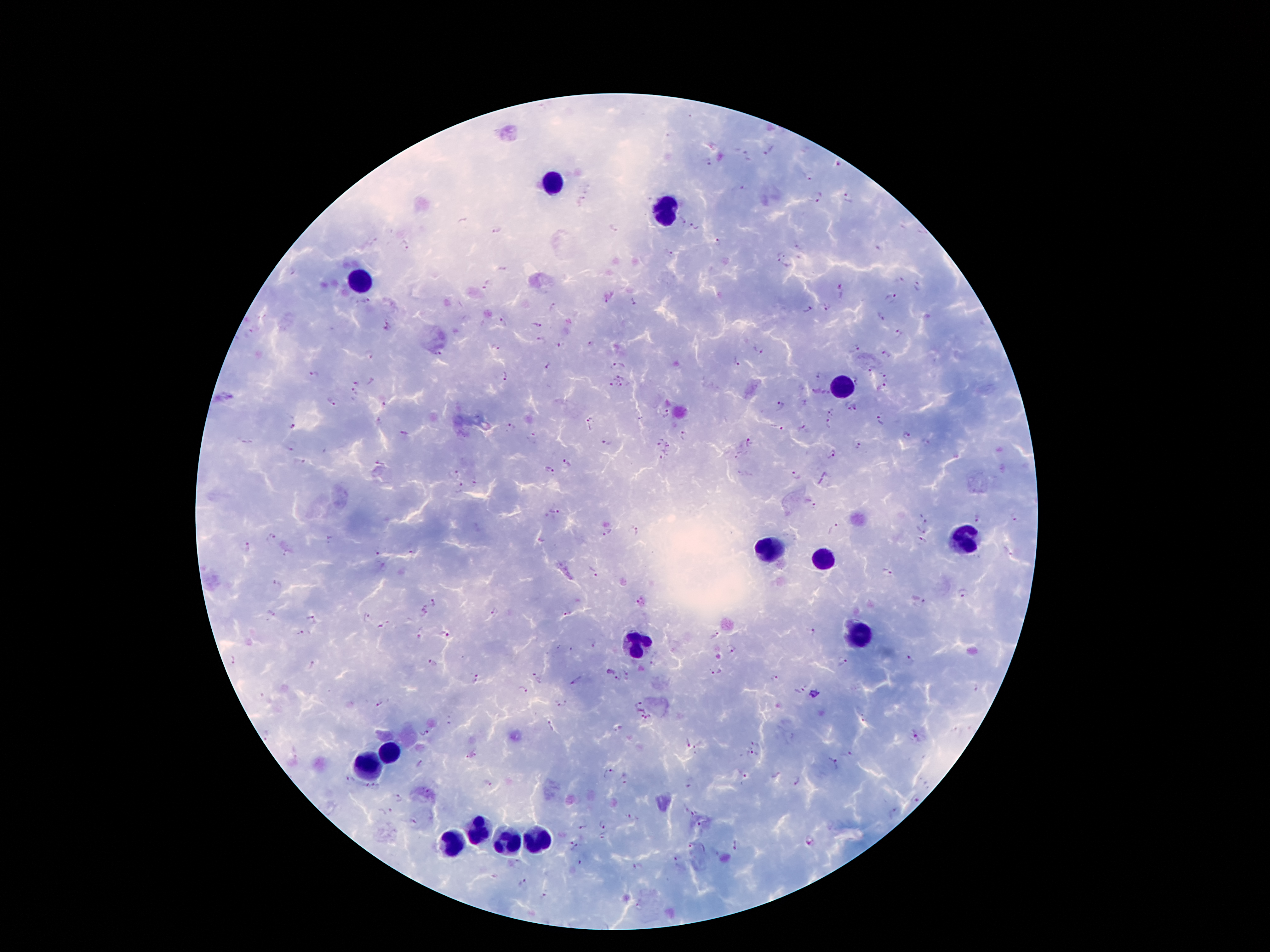

Approximate centers as [x, y] in pixels.
Summary:
  - Plasmodium parasite locations: [769, 152], [746, 157], [707, 163], [839, 165], [810, 177], [820, 197], [849, 197], [580, 200], [462, 221], [683, 221], [694, 226], [614, 228], [497, 231], [718, 243], [404, 247], [782, 250], [879, 251], [672, 252], [782, 265], [503, 270], [901, 279], [487, 284], [919, 285], [842, 291], [891, 296], [609, 298], [635, 300], [552, 304], [827, 308], [806, 310], [881, 316], [504, 323], [535, 326], [388, 328], [900, 333], [541, 341], [590, 343], [561, 346], [496, 348], [757, 348], [857, 348], [368, 354], [438, 354], [887, 354], [620, 362], [736, 362], [548, 366], [872, 368], [315, 373], [817, 374], [883, 374], [623, 375], [505, 378], [857, 380], [355, 383], [613, 384], [623, 386], [883, 387], [815, 391], [354, 392], [828, 392], [332, 402], [385, 404], [780, 405], [857, 406], [846, 407], [831, 411], [667, 412], [881, 419], [591, 423], [828, 425], [291, 426], [511, 427], [777, 429], [804, 429], [404, 434], [684, 434], [907, 436], [533, 438], [660, 439], [750, 440], [244, 442], [608, 442], [858, 444], [669, 445], [290, 449], [831, 454], [665, 455], [740, 455], [298, 463], [381, 463], [567, 463], [549, 471], [454, 474], [797, 475], [476, 482], [462, 490], [810, 503], [554, 509], [978, 517], [1014, 518], [922, 519], [834, 529], [921, 529], [635, 531], [607, 534], [270, 537], [330, 541], [921, 543], [246, 547], [1008, 552], [378, 553], [286, 554], [887, 572], [592, 573], [278, 585], [964, 594], [920, 600], [640, 601], [433, 603], [269, 613], [494, 613], [567, 613], [423, 614], [313, 618], [364, 618], [381, 627], [811, 632], [300, 634], [446, 635], [715, 635], [591, 646], [731, 649], [232, 660], [908, 660], [842, 661], [432, 663], [312, 665], [716, 672], [617, 677], [536, 678], [775, 678], [476, 681], [575, 681], [522, 690], [800, 691], [379, 703], [559, 705], [639, 707], [646, 719], [550, 725], [424, 733], [267, 736], [916, 737], [687, 743], [757, 743], [848, 754], [473, 755], [751, 755], [834, 762], [421, 765], [605, 772], [742, 773], [624, 780], [797, 780], [349, 781], [488, 783], [370, 789], [690, 789], [398, 798], [915, 800], [387, 812], [692, 814], [635, 819], [412, 822], [601, 823], [700, 825], [583, 827], [603, 837], [810, 842], [736, 845], [573, 846], [691, 847], [677, 863], [581, 864], [637, 866], [523, 882], [544, 896], [639, 906]
  - Leukocyte locations: [555, 184], [664, 206], [359, 279], [837, 383], [961, 537], [770, 548], [823, 556], [857, 635], [639, 640], [389, 755], [364, 760], [479, 831], [532, 836], [454, 839], [507, 842]
  - Preparation: thick blood smear
  - Patient malaria status: positive for Plasmodium falciparum
  - Field of view: one from this slide
  - Capture: smartphone through the microscope eyepiece
  - Stain: Giemsa
  - Magnification: 100x
  - Image size: 1270×952 pixels